Report the malaria status of this cell.
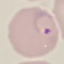
Parasitized.

Summary:
  - Preparation: thin blood smear
  - Stain: Giemsa
  - Image type: automatically extracted cell patch, resized to 64 × 64 pixels
  - Capture: smartphone camera at the microscope eyepiece